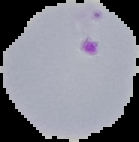

result: Plasmodium parasites identified
image_size: 139×142 pixels
preparation: thin blood smear
image_type: segmented cell region with the area outside set to black